Identify the parasite.
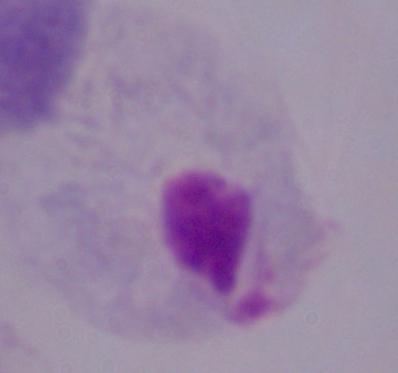

A trichomonad.

magnification = 1000x
modality = micrograph